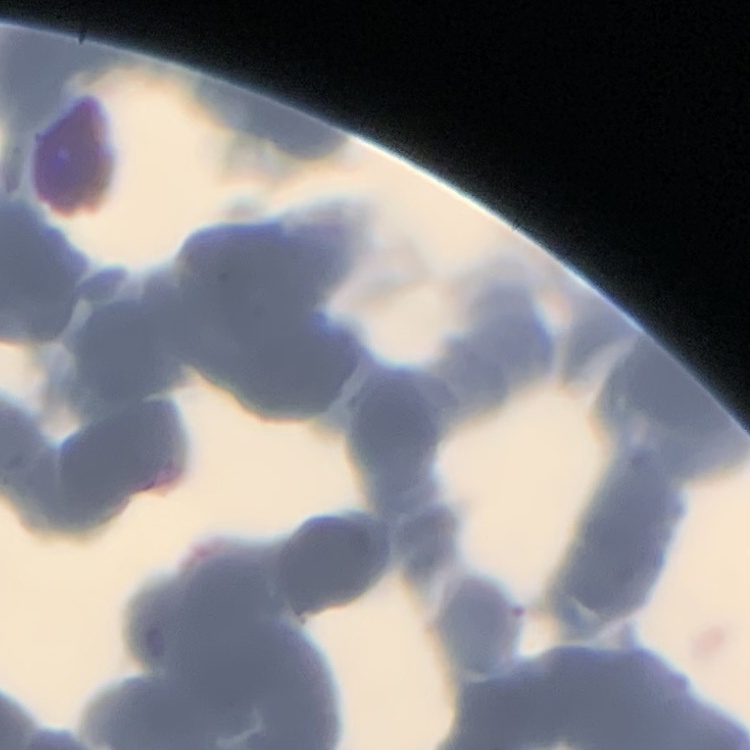

erythrocyte morphology = rouleaux formation
image type = one tile cut from a larger photomicrograph
stain = Field's or Giemsa
preparation = thin blood smear